Classify this cell by malaria status.
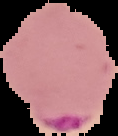

It is parasitized.

preparation = thin blood smear
image type = segmented cell region with the area outside set to black
image size = 118×136 pixels